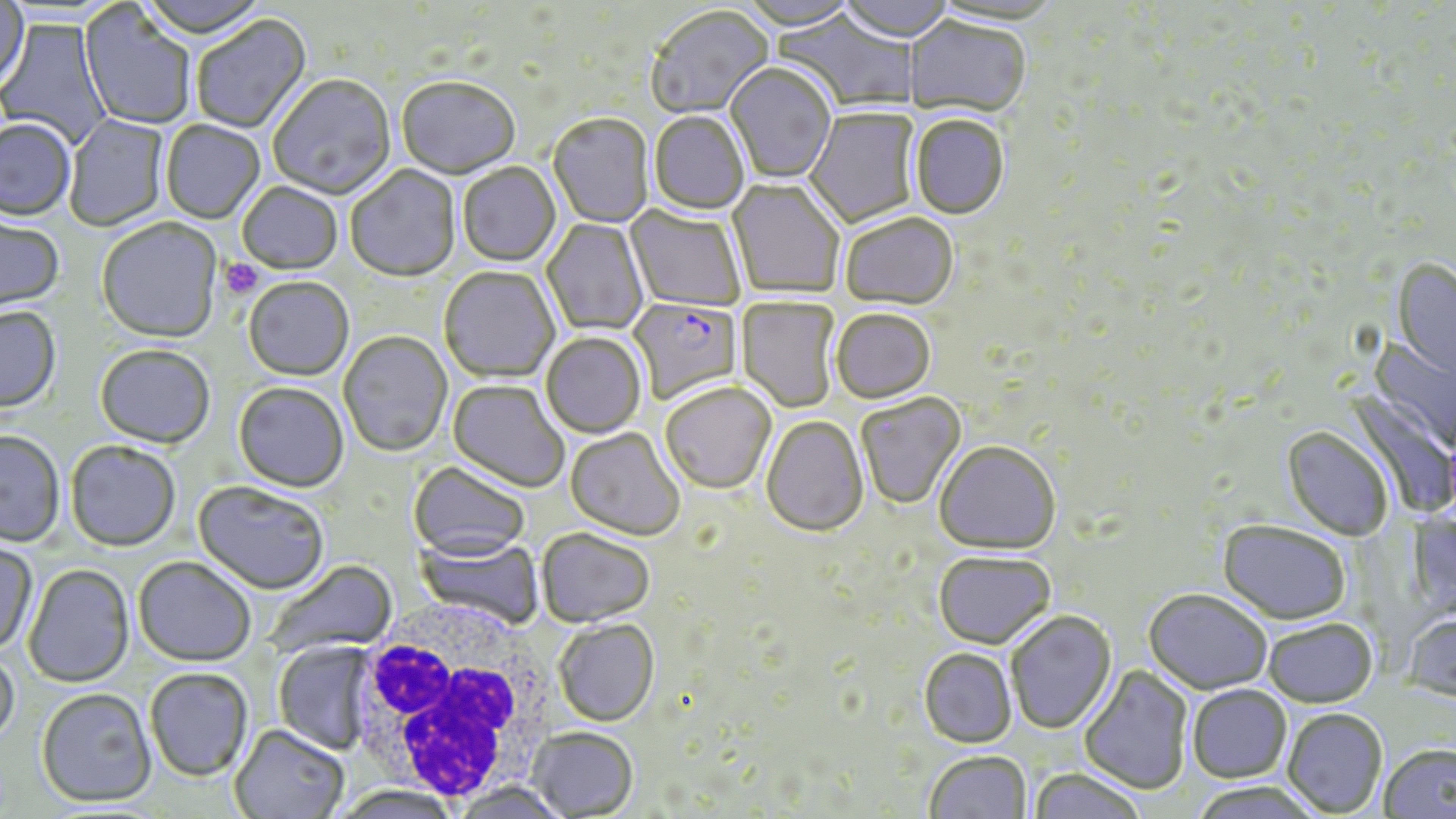
slide-level diagnosis = Plasmodium falciparum
magnification = 1000x
image size = 1456×819 pixels
modality = light microscopy
platelet locations = approximate bounding boxes as [x1, y1, x2, y2] in pixels: [219, 258, 264, 299]
field of view = single
uninfected red blood cell locations = approximate bounding boxes as [x1, y1, x2, y2] in pixels: [136, 0, 272, 42], [737, 0, 858, 32], [836, 0, 956, 45], [930, 1, 1065, 30], [0, 2, 31, 96], [79, 4, 195, 130], [646, 7, 774, 120], [775, 9, 918, 113], [191, 15, 312, 136], [0, 18, 113, 149], [904, 18, 1030, 119], [725, 64, 836, 185], [268, 76, 396, 202], [397, 79, 520, 182], [805, 108, 922, 229], [648, 113, 750, 217], [64, 115, 170, 231], [548, 115, 654, 229], [909, 117, 1010, 221], [0, 120, 76, 223], [160, 121, 265, 224], [458, 163, 561, 268], [345, 166, 461, 283], [727, 179, 844, 299], [237, 183, 343, 276], [625, 206, 746, 312], [840, 215, 959, 312], [0, 216, 64, 314], [541, 219, 649, 337], [97, 220, 223, 345], [1390, 259, 1456, 383], [439, 267, 560, 385], [243, 278, 354, 382], [736, 296, 840, 413], [0, 307, 62, 414], [830, 310, 936, 405], [338, 332, 453, 458], [540, 333, 646, 439], [1367, 335, 1455, 454], [95, 346, 215, 451], [447, 380, 570, 493], [233, 383, 349, 494], [660, 383, 776, 494], [1346, 391, 1455, 519], [856, 394, 967, 511], [761, 416, 869, 538], [1282, 427, 1393, 541], [566, 428, 684, 542], [0, 431, 65, 548], [65, 442, 180, 553], [934, 442, 1060, 556], [409, 461, 531, 562], [193, 481, 329, 596], [1217, 521, 1351, 625], [536, 528, 655, 628], [415, 535, 545, 630], [0, 541, 38, 656], [933, 552, 1055, 650], [133, 557, 256, 667], [264, 560, 397, 658], [23, 564, 135, 689], [1143, 589, 1272, 695], [1006, 611, 1117, 734], [1402, 612, 1456, 704], [1262, 618, 1377, 708], [554, 620, 659, 727], [273, 641, 377, 754], [0, 647, 21, 752], [918, 648, 1017, 748], [1079, 665, 1193, 795], [145, 668, 253, 783], [1187, 684, 1292, 783], [36, 689, 157, 809], [1282, 708, 1387, 817], [229, 724, 349, 818], [528, 726, 638, 818], [1378, 743, 1455, 818], [924, 751, 1032, 819], [1027, 769, 1148, 819], [453, 781, 572, 818], [335, 785, 461, 819]
preparation = thin blood smear
stain = May-Grünwald-Giemsa
Plasmodium falciparum-infected red blood cell locations = approximate bounding boxes as [x1, y1, x2, y2] in pixels: [627, 299, 744, 406]
white blood cell locations = approximate bounding boxes as [x1, y1, x2, y2] in pixels: [346, 618, 553, 807]